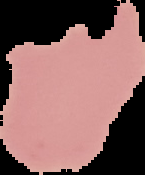

preparation = thin blood film
image size = 145×175 pixels
image type = segmented cell region with the area outside set to black
result = malaria parasites identified